Report the malaria status of this cell.
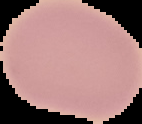
It is uninfected.

Summary:
  - Image size: 142×124 pixels
  - Image type: segmented cell region on a black background
  - Preparation: thin blood smear